Locate every Plasmodium parasite.
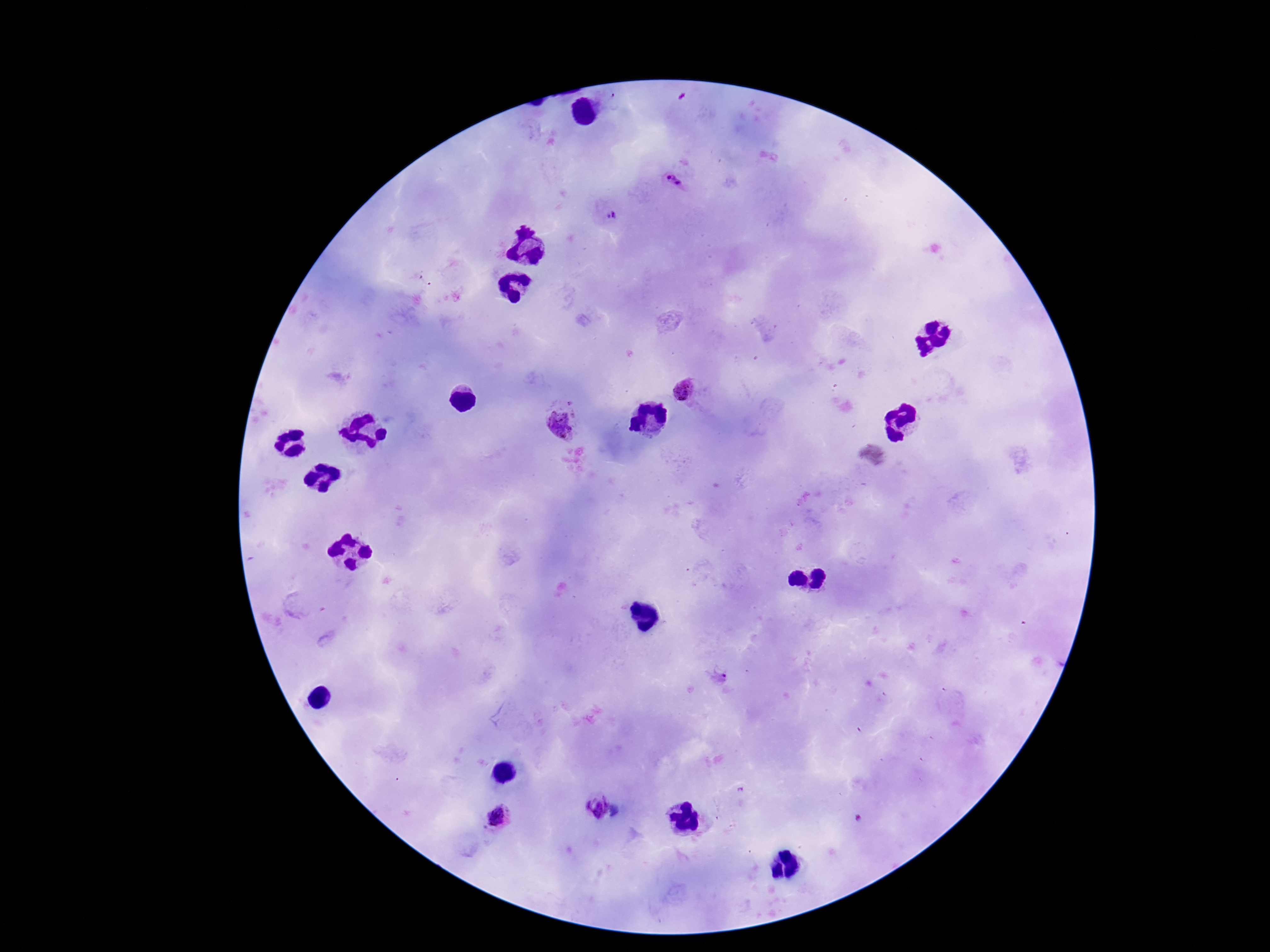

Approximate centers as [x, y] in pixels.
Plasmodium parasites: [674, 181], [613, 216], [683, 390], [558, 422], [719, 677], [594, 805], [499, 817].

Thick blood smear. Smartphone photograph taken through the microscope eyepiece. Patient malaria status: infected. Image is 1270×952 pixels. One field from this slide. Giemsa stain. 100x magnification.